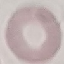

Malaria status: uninfected. Automatically extracted cell patch, resized to 64 × 64 pixels. Giemsa-stained preparation. Acquired by smartphone through the microscope eyepiece. Thin smear of blood.